Locate every blood parasite and identify its species.
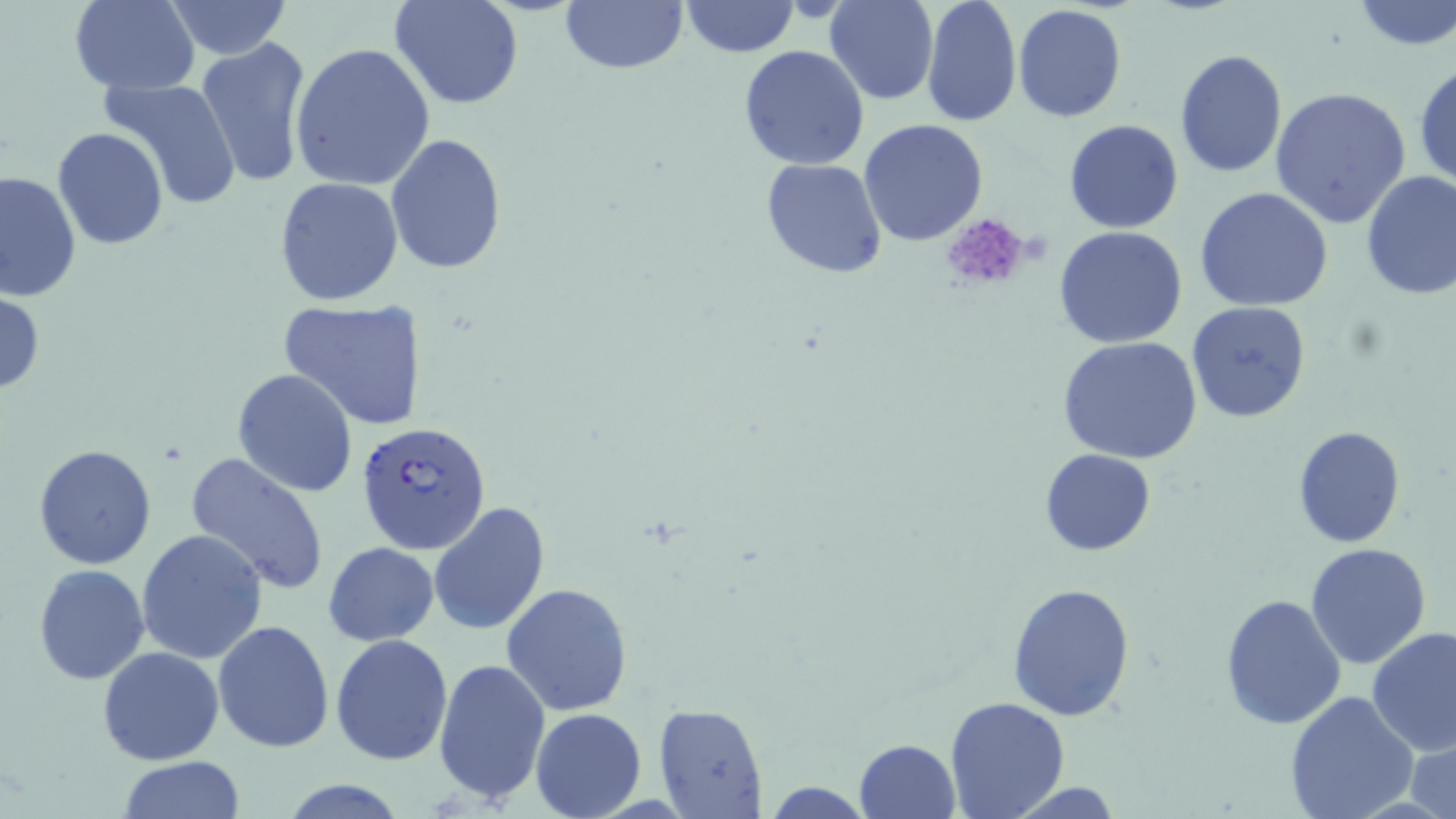

Approximate bounding boxes as named x1/y1/x2/y2 corners in pixels.
Plasmodium falciparum-infected red blood cells: (x1=358, y1=420, x2=491, y2=555).
No Plasmodium ovale, Plasmodium malariae, Plasmodium vivax, Babesia divergens, or Trypanosoma brucei observed.

Uninfected red blood cell locations: (x1=162, y1=0, x2=292, y2=60), (x1=390, y1=0, x2=524, y2=109), (x1=559, y1=0, x2=689, y2=75), (x1=679, y1=0, x2=799, y2=57), (x1=826, y1=0, x2=938, y2=105), (x1=920, y1=0, x2=1022, y2=127), (x1=1349, y1=0, x2=1456, y2=50), (x1=68, y1=1, x2=199, y2=93), (x1=1011, y1=4, x2=1130, y2=123), (x1=195, y1=36, x2=313, y2=191), (x1=290, y1=42, x2=436, y2=190), (x1=738, y1=45, x2=871, y2=171), (x1=1174, y1=48, x2=1287, y2=178), (x1=1412, y1=59, x2=1456, y2=190), (x1=103, y1=78, x2=244, y2=211), (x1=1270, y1=88, x2=1413, y2=230), (x1=858, y1=117, x2=988, y2=247), (x1=1063, y1=120, x2=1185, y2=234), (x1=50, y1=126, x2=169, y2=252), (x1=385, y1=132, x2=508, y2=275), (x1=760, y1=156, x2=888, y2=279), (x1=0, y1=169, x2=80, y2=304), (x1=1359, y1=170, x2=1456, y2=300), (x1=275, y1=177, x2=403, y2=305), (x1=1193, y1=188, x2=1335, y2=313), (x1=1053, y1=226, x2=1189, y2=349), (x1=0, y1=288, x2=46, y2=399), (x1=278, y1=299, x2=427, y2=432), (x1=1185, y1=301, x2=1313, y2=422), (x1=1057, y1=336, x2=1207, y2=465), (x1=232, y1=368, x2=358, y2=497), (x1=1292, y1=425, x2=1406, y2=547), (x1=33, y1=444, x2=158, y2=570), (x1=1040, y1=448, x2=1155, y2=555), (x1=184, y1=450, x2=331, y2=597), (x1=428, y1=500, x2=550, y2=636), (x1=137, y1=528, x2=268, y2=664), (x1=323, y1=541, x2=439, y2=645), (x1=1305, y1=542, x2=1433, y2=670), (x1=32, y1=563, x2=152, y2=685), (x1=501, y1=582, x2=633, y2=715), (x1=1007, y1=582, x2=1137, y2=723), (x1=1220, y1=592, x2=1348, y2=729), (x1=213, y1=620, x2=336, y2=754), (x1=1367, y1=626, x2=1456, y2=756), (x1=331, y1=633, x2=453, y2=765), (x1=1327, y1=639, x2=1445, y2=790), (x1=97, y1=646, x2=224, y2=767), (x1=433, y1=657, x2=551, y2=806), (x1=1283, y1=690, x2=1418, y2=819), (x1=943, y1=697, x2=1071, y2=818), (x1=653, y1=703, x2=768, y2=818), (x1=530, y1=706, x2=647, y2=819), (x1=1410, y1=733, x2=1456, y2=819), (x1=853, y1=738, x2=961, y2=819), (x1=118, y1=756, x2=244, y2=819), (x1=277, y1=778, x2=411, y2=818), (x1=1000, y1=781, x2=1129, y2=817). Platelet locations: (x1=940, y1=213, x2=1034, y2=291). Slide-level diagnosis: Plasmodium falciparum. Thin blood smear. May-Grünwald-Giemsa stain. Captured at 1000x magnification. One field of a larger specimen. Image is 1456×819 pixels. Optical microscopy.